Report the malaria status of this cell.
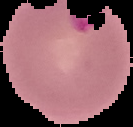

Parasitized.

Summary:
  - Image type: cell region segmented out of the field of view; surrounding area masked to black
  - Image size: 133×127 pixels
  - Preparation: thin blood film